State the preparation type.
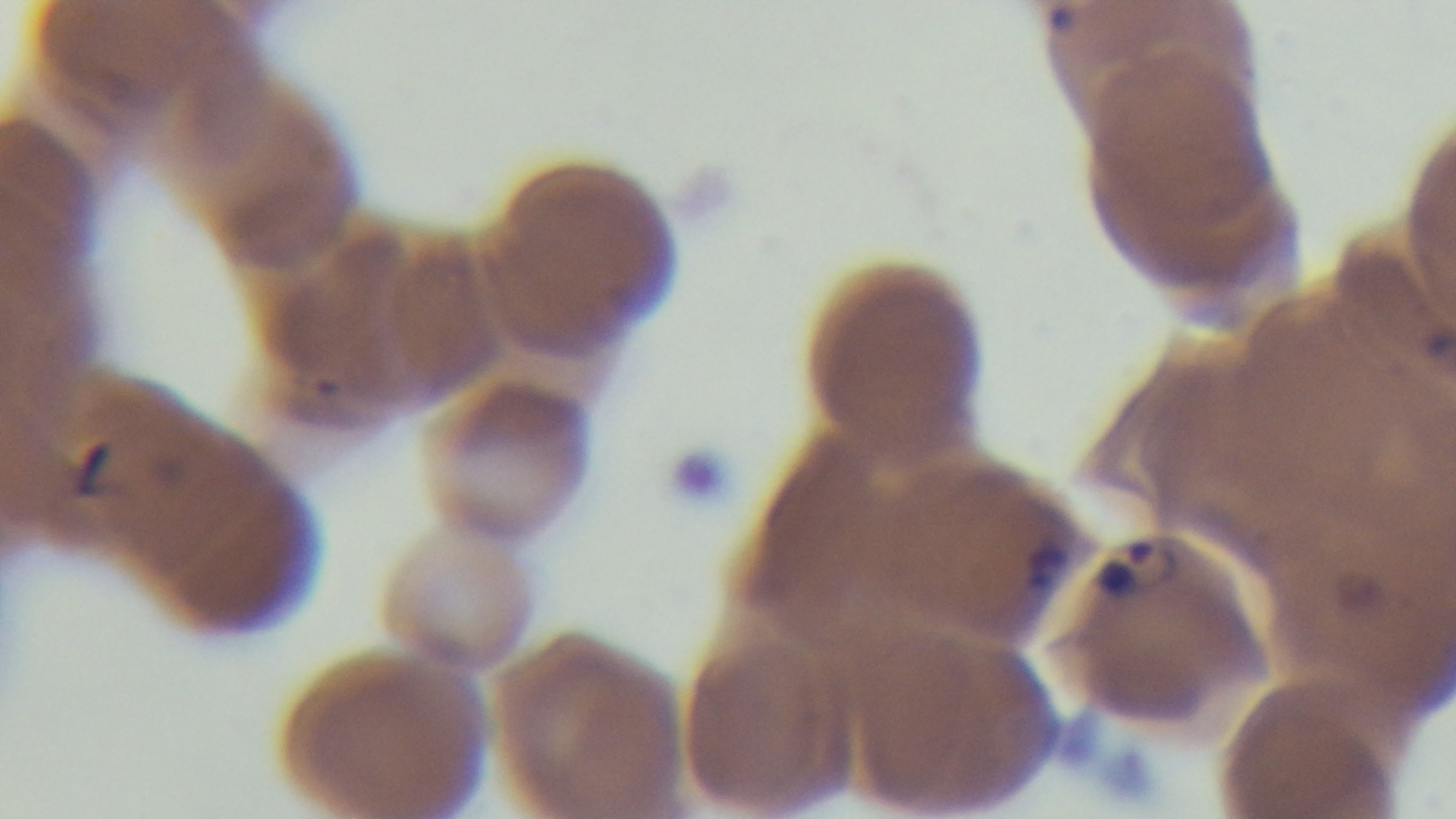

Thin.

Summary:
  - Malaria status: positive
  - Stain: Giemsa
  - Modality: light microscopy
  - Capture: mounted 4K digital camera
  - Objective: 100x oil immersion
  - Field of view: one from the slide